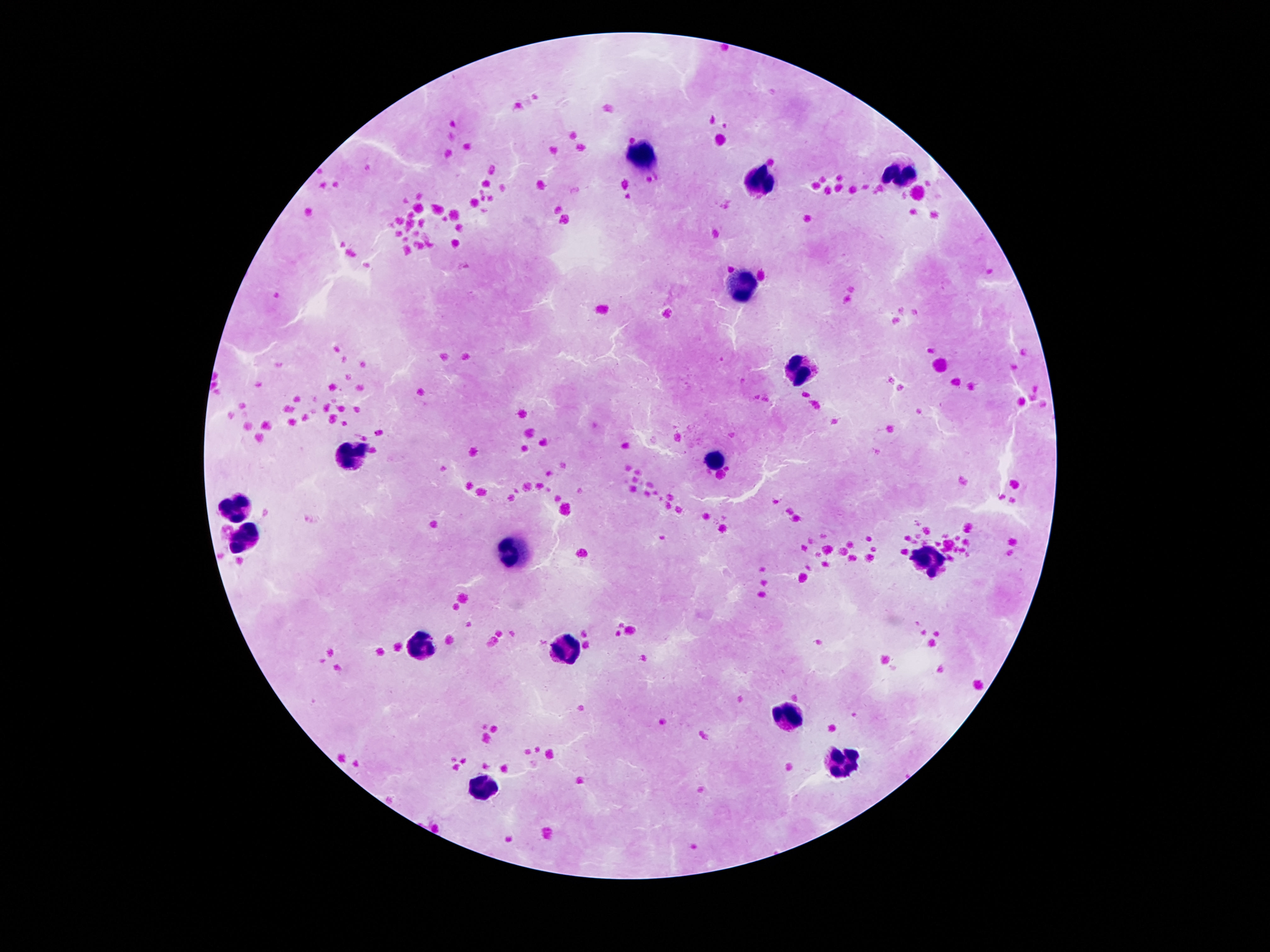
magnification = 100x
leukocyte locations = approximate object centers, in pixels from the top-left corner: (x=646, y=159), (x=902, y=173), (x=758, y=185), (x=744, y=288), (x=802, y=371), (x=354, y=453), (x=718, y=460), (x=237, y=509), (x=247, y=532), (x=515, y=554), (x=930, y=563), (x=424, y=646), (x=566, y=649), (x=793, y=715), (x=842, y=764), (x=489, y=786)
preparation = thick blood film
patient malaria status = negative
capture = smartphone camera through the microscope eyepiece
image size = 1270×952 pixels
field of view = single
stain = Giemsa